Give the position of every leukocyte visible.
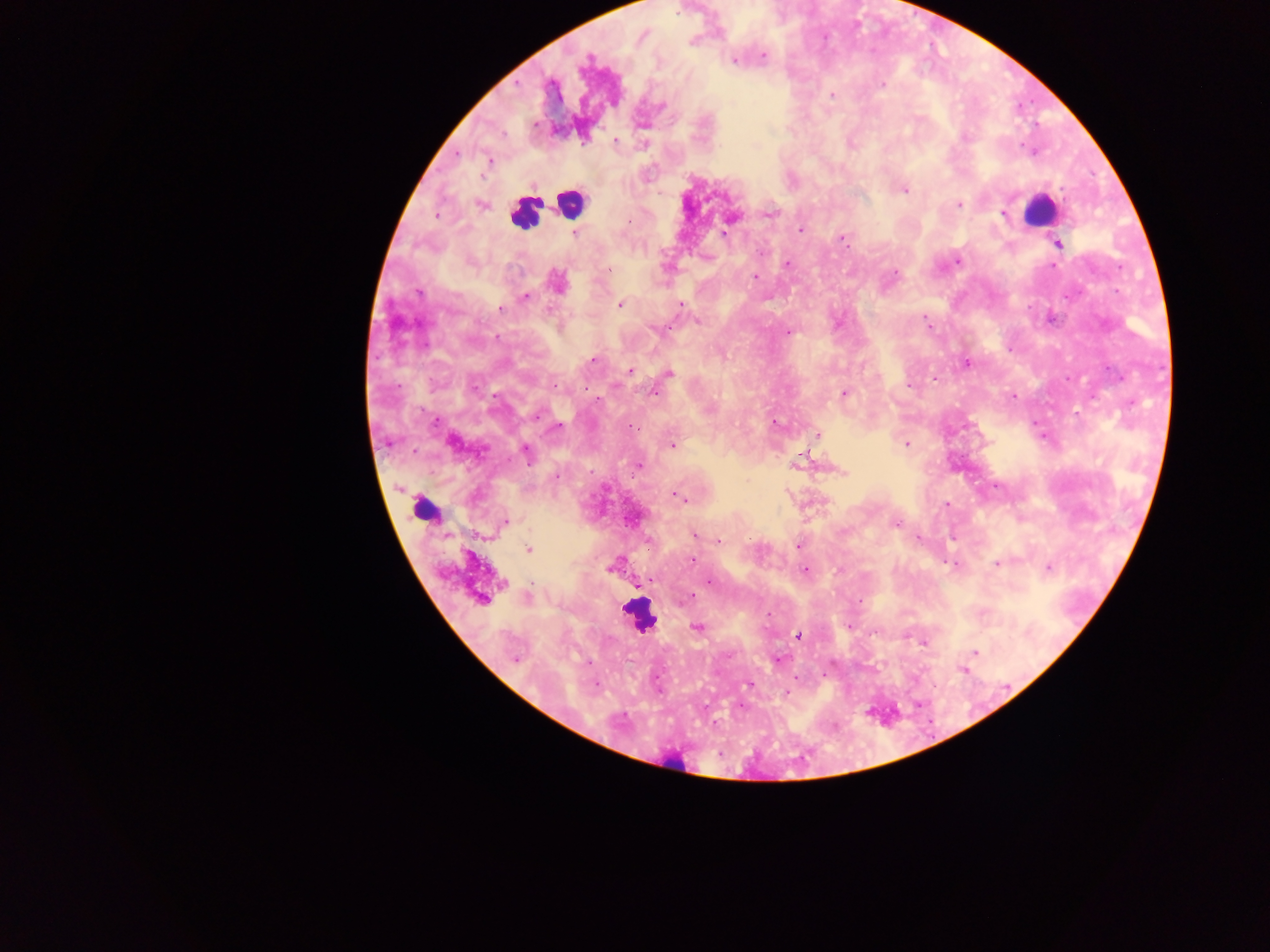

Approximate centers as [x, y] in pixels.
Leukocytes: [570, 203], [1039, 210], [525, 215], [423, 509], [638, 616], [676, 762].

preparation = thick blood smear
capture = mobile-phone photograph through a microscope
country = Ghana
image size = 1270×952 pixels
Plasmodium parasite locations = approximate centers as [x, y] in pixels: [692, 42], [763, 55], [734, 61], [883, 84], [833, 95], [965, 136], [616, 140], [488, 161], [905, 191], [481, 205], [959, 205], [769, 214], [1003, 214], [436, 215], [731, 217], [629, 221], [726, 229], [801, 231], [574, 233], [724, 234], [842, 240], [1057, 244], [958, 261], [787, 264], [1053, 267], [609, 270], [895, 272], [756, 276], [559, 282], [417, 293], [525, 297], [680, 304], [620, 305], [500, 308], [926, 320], [698, 321], [660, 330], [788, 332], [593, 360], [967, 363], [629, 371], [670, 374], [934, 378], [554, 385], [908, 386], [474, 387], [654, 394], [844, 394], [1013, 397], [596, 398], [537, 415], [775, 422], [632, 427], [557, 428], [817, 435], [452, 441], [906, 444], [673, 445], [526, 453], [639, 466], [841, 472], [556, 477], [676, 495], [947, 505], [506, 521], [896, 524], [694, 536], [648, 540], [719, 540], [798, 545], [528, 549], [693, 560], [997, 563], [610, 568], [1048, 568], [806, 571], [650, 580], [709, 581], [528, 597], [690, 598], [481, 600], [698, 627], [798, 635], [923, 642], [975, 651], [515, 659], [778, 659], [962, 670], [748, 684], [596, 685], [786, 693]
field of view = single